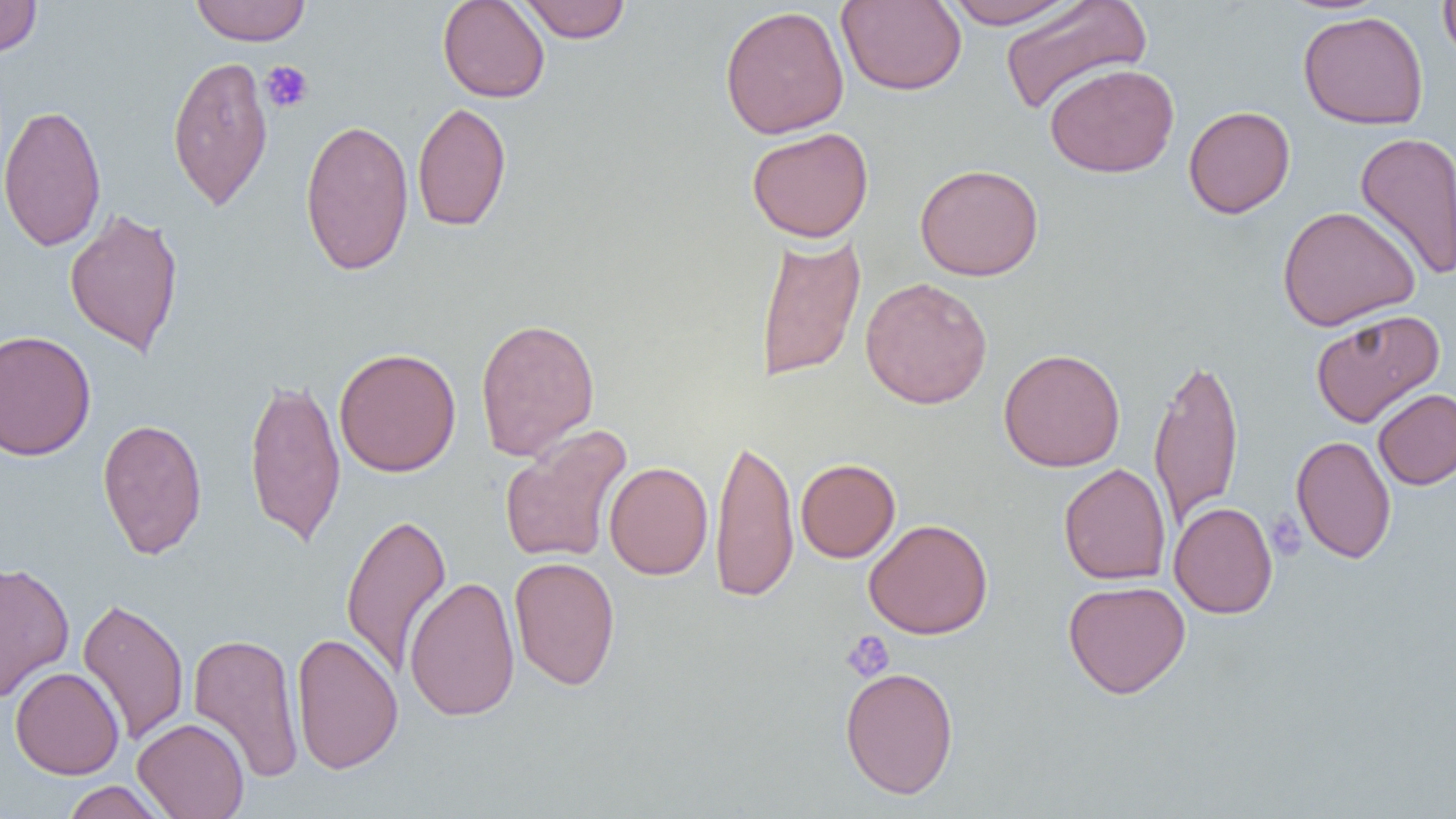

slide-level diagnosis = no evidence of blood parasites
uninfected red blood cell locations = approximate bounding boxes as (x1, y1, x2, y2) in pixels: (0, 0, 43, 59), (437, 0, 550, 103), (517, 0, 632, 43), (836, 0, 967, 96), (942, 0, 1082, 29), (1438, 0, 1456, 66), (190, 1, 311, 46), (998, 1, 1152, 117), (719, 4, 850, 139), (1298, 10, 1429, 130), (167, 55, 274, 211), (1044, 62, 1180, 177), (412, 101, 512, 233), (0, 103, 107, 252), (1183, 105, 1296, 218), (300, 118, 414, 276), (746, 126, 874, 243), (1354, 131, 1456, 282), (914, 163, 1044, 281), (1277, 205, 1420, 331), (64, 208, 185, 357), (754, 232, 866, 383), (860, 277, 993, 409), (1310, 308, 1445, 428), (475, 317, 600, 461), (0, 330, 96, 460), (333, 347, 461, 477), (998, 348, 1126, 472), (1149, 354, 1244, 528), (243, 374, 346, 548), (1373, 388, 1456, 490), (97, 417, 208, 560), (498, 425, 633, 564), (710, 433, 799, 604), (1291, 434, 1396, 564), (796, 458, 900, 562), (604, 461, 713, 580), (1058, 463, 1171, 585), (1169, 502, 1278, 618), (341, 511, 452, 679), (864, 518, 993, 639), (508, 556, 621, 691), (0, 561, 74, 702), (404, 574, 520, 722), (1063, 579, 1191, 698), (77, 596, 189, 747), (187, 632, 305, 784), (291, 632, 403, 774), (10, 666, 124, 779), (840, 666, 959, 799), (133, 717, 249, 819), (61, 780, 168, 818)
platelet locations = approximate bounding boxes as (x1, y1, x2, y2) in pixels: (260, 61, 314, 113), (1266, 510, 1307, 560), (840, 630, 895, 682)
image size = 1456×819 pixels
modality = light microscopy
field of view = single
magnification = 1000x
preparation = thin blood smear